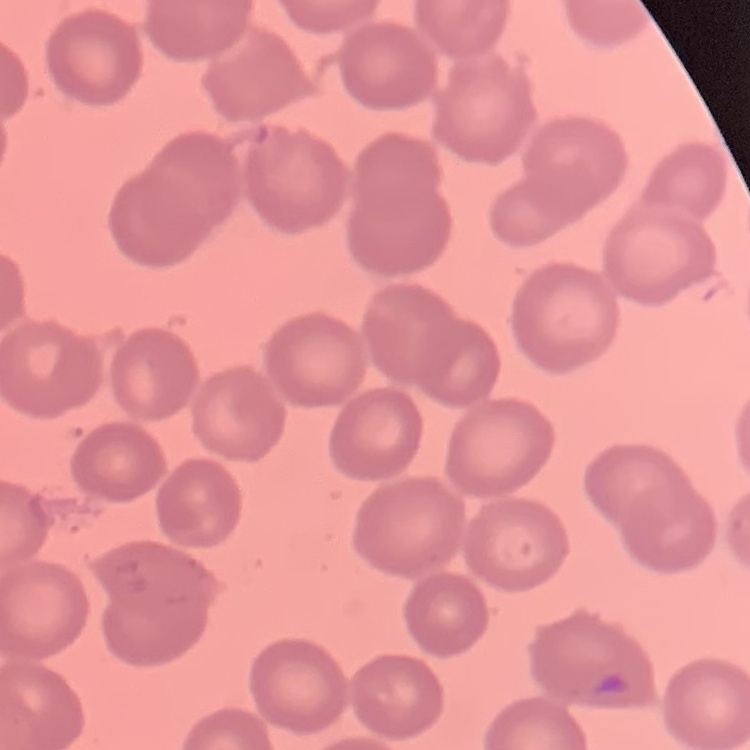

erythrocyte_morphology: no rouleaux formation
stain: Field's or Giemsa
preparation: thin blood film
image_type: square crop of a larger photomicrograph